Classify this cell by malaria status.
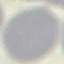

Uninfected.

Giemsa-stained preparation. Cell patch, automatically extracted from a larger field of view and resized to 64 × 64 pixels. Thin blood film. Photographed with a smartphone camera at the microscope eyepiece.